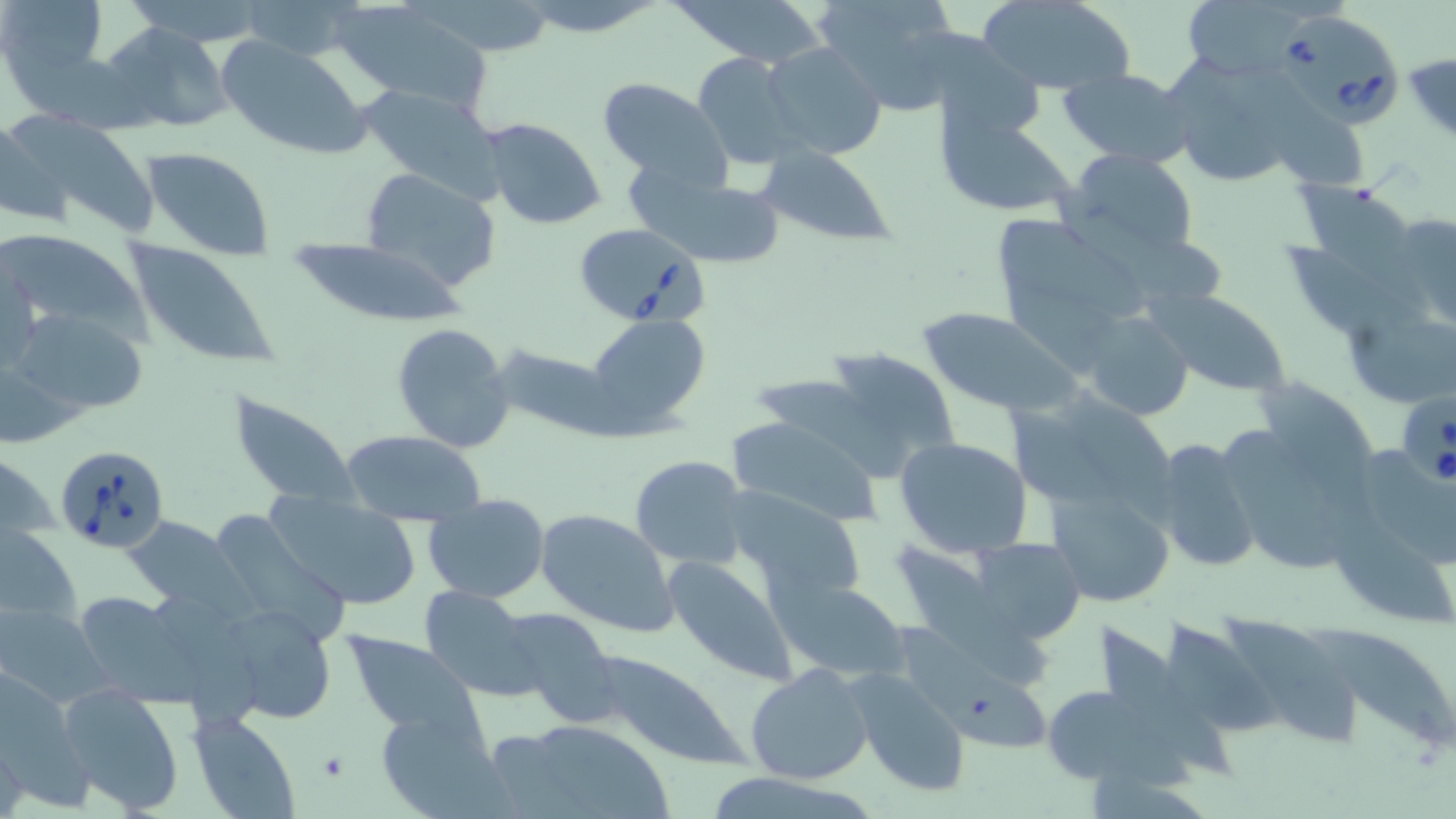
Approximate bounding boxes as (x1, y1, x2, y2) in pixels. Babesia divergens-infected red blood cell locations: (1277, 14, 1404, 128), (573, 219, 708, 327), (1401, 386, 1455, 491), (55, 444, 172, 555). Platelet locations: (316, 750, 350, 784). Uninfected red blood cell locations: (241, 0, 371, 62), (520, 0, 663, 36), (676, 0, 827, 66), (812, 0, 961, 115), (974, 0, 1134, 94), (0, 1, 112, 99), (1177, 1, 1316, 78), (335, 2, 492, 109), (426, 2, 562, 57), (98, 21, 236, 135), (216, 36, 373, 161), (761, 41, 887, 162), (694, 51, 802, 168), (1404, 51, 1456, 146), (1166, 57, 1310, 189), (1059, 68, 1192, 166), (594, 76, 729, 183), (357, 83, 506, 197), (1266, 99, 1371, 192), (0, 113, 96, 231), (937, 113, 1075, 219), (480, 118, 608, 231), (140, 146, 275, 260), (755, 147, 897, 247), (1061, 148, 1202, 262), (359, 167, 501, 291), (634, 168, 790, 268), (1297, 184, 1432, 319), (1391, 210, 1456, 330), (995, 214, 1143, 324), (0, 228, 152, 345), (122, 239, 279, 369), (288, 239, 467, 327), (1, 252, 45, 377), (1150, 288, 1290, 397), (9, 307, 153, 421), (918, 308, 1084, 417), (1080, 310, 1195, 421), (585, 313, 710, 433), (391, 323, 515, 454), (494, 343, 619, 440), (810, 346, 961, 482), (0, 353, 93, 450), (1261, 373, 1377, 518), (229, 389, 358, 508), (1067, 391, 1193, 522), (724, 414, 885, 526), (1231, 423, 1354, 569), (340, 430, 488, 525), (895, 436, 1034, 558), (1149, 436, 1264, 575), (1368, 441, 1456, 571), (629, 455, 750, 570), (1048, 483, 1178, 605), (721, 488, 868, 599), (263, 490, 424, 610), (424, 494, 549, 603), (1337, 504, 1456, 628), (535, 508, 678, 636), (124, 514, 241, 608), (0, 522, 81, 630), (888, 537, 1051, 689), (976, 539, 1090, 642), (665, 555, 796, 685), (771, 576, 908, 680), (421, 586, 541, 701), (65, 589, 200, 701), (215, 601, 337, 723), (1, 603, 112, 707), (496, 605, 621, 727), (1227, 610, 1360, 746), (1159, 615, 1274, 741), (1102, 620, 1234, 778), (1308, 624, 1456, 748), (343, 633, 483, 736), (587, 650, 743, 765), (745, 664, 874, 785), (847, 668, 973, 799), (951, 677, 1050, 751), (58, 684, 185, 814), (1043, 685, 1161, 783), (377, 707, 507, 816), (189, 713, 299, 819), (506, 720, 676, 819), (699, 769, 876, 819). Slide-level diagnosis: Babesia divergens. Thin blood smear. Image is 1456×819 pixels. 1000x magnification. May-Grünwald-Giemsa stain. Optical microscopy. Single field of view.